Assess this cell for malaria.
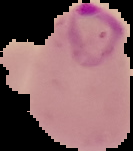
It is parasitized.

image_type: segmented cell region with the area outside set to black
image_size: 133×151 pixels
preparation: thin blood film